Report the malaria status of this cell.
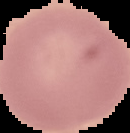
Uninfected.

Image is 130×133 pixels. Cell region segmented out of the field of view; the surrounding area is masked to black. From a thin blood smear.